Identify the parasite.
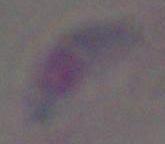

Toxoplasma gondii.

Captured at 1000x magnification. Micrograph.